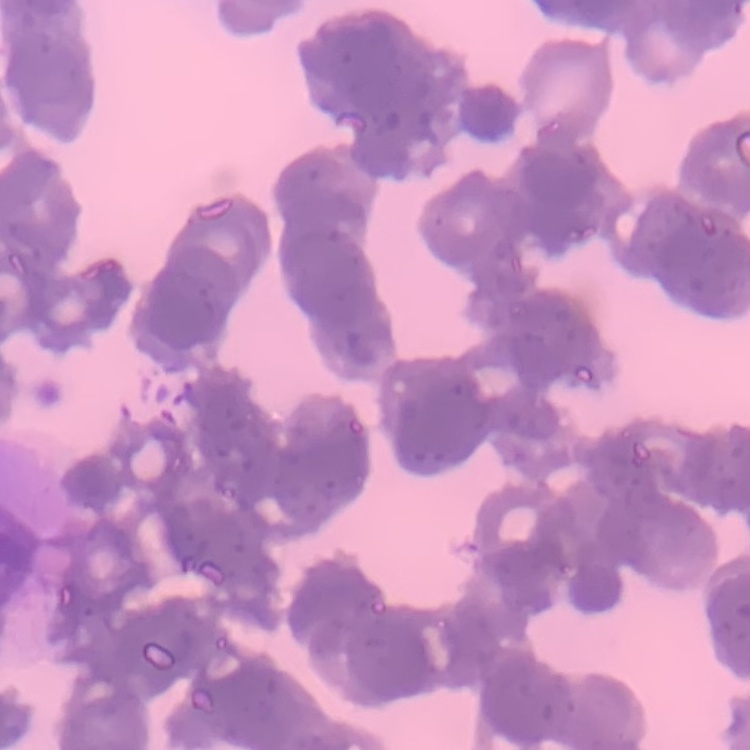

Summary:
  - Red blood cell morphology: rouleaux formation
  - Preparation: thin blood film
  - Image type: one tile cut from a larger photomicrograph
  - Stain: Field's or Giemsa